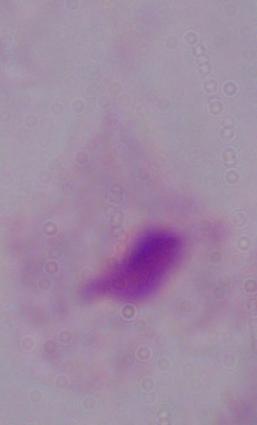

{
  "magnification": "1000x",
  "identification": "trichomonad",
  "modality": "micrograph"
}